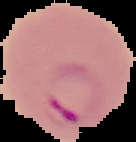

Summary:
  - Preparation: thin blood film
  - Image type: segmented cell region on a black background
  - Malaria status: parasitized
  - Image size: 136×142 pixels